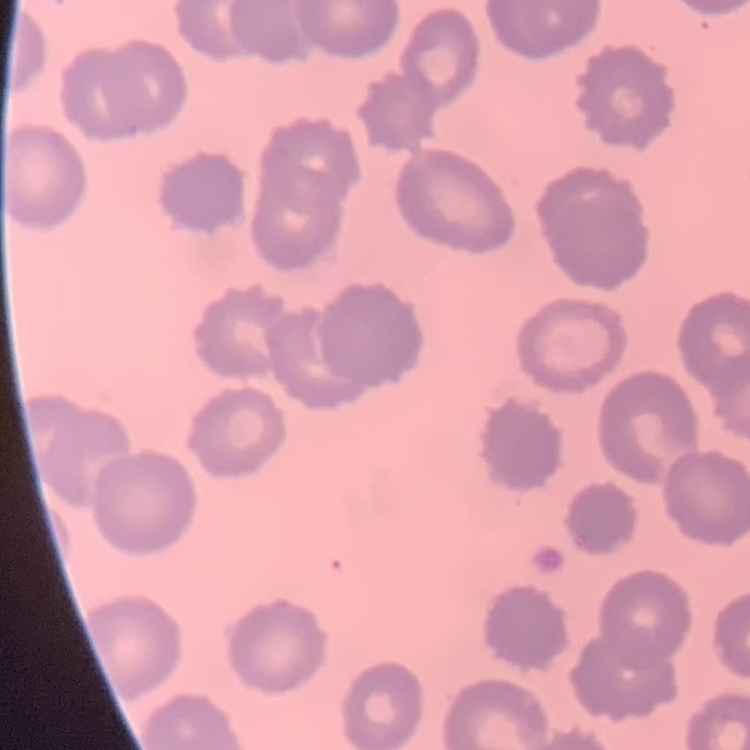

The red blood cells exhibit no rouleaux formation. Stained with either Field's or Giemsa. Thin peripheral smear. Square crop of a larger photomicrograph.